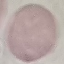
Malaria status: uninfected. Giemsa stain. Photographed with a smartphone camera at the microscope eyepiece. Thin smear of blood. Cell patch, automatically extracted from a larger field of view and resized to 64 × 64 pixels.